Locate every Plasmodium parasite.
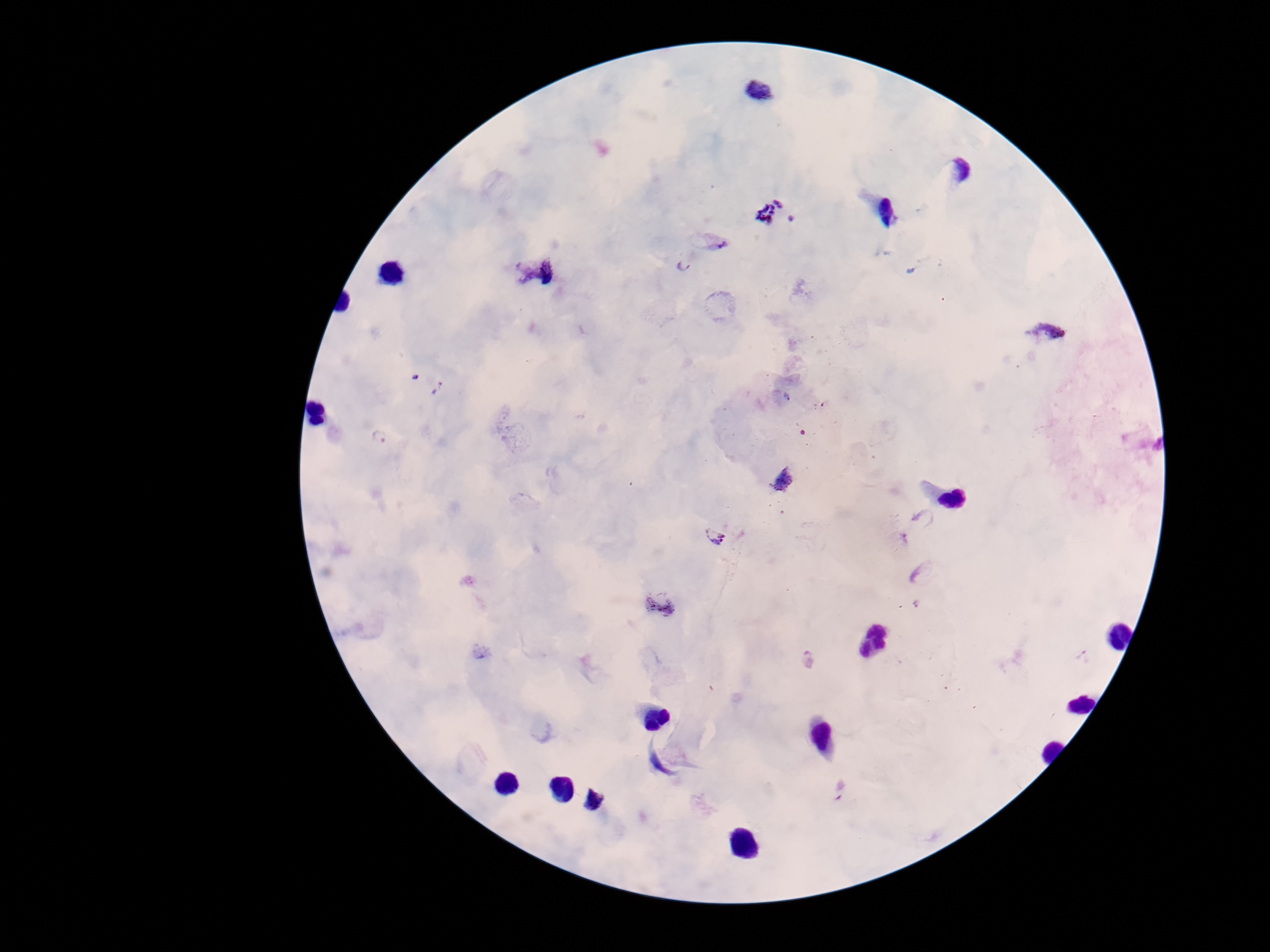
Approximate object centers, in pixels from the top-left corner.
Plasmodium parasites: (x=758, y=92), (x=958, y=169), (x=775, y=215), (x=713, y=240), (x=682, y=265), (x=537, y=271), (x=1050, y=335), (x=378, y=438), (x=784, y=481), (x=715, y=536), (x=658, y=605), (x=918, y=605), (x=1084, y=657), (x=808, y=661), (x=840, y=790), (x=593, y=799).

Summary:
  - Patient malaria status: infected
  - Preparation: thick peripheral-blood smear
  - Magnification: 100x
  - Field of view: single
  - Image size: 1270×952 pixels
  - Stain: Giemsa
  - Capture: smartphone camera through the microscope eyepiece